State which parasite is depicted.
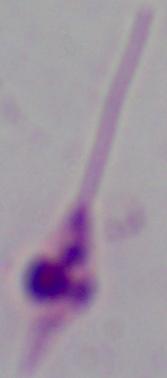
Leishmania.

Captured at 1000x magnification. Photomicrograph.